Report the malaria status of this cell.
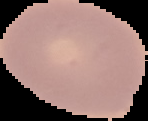
It is uninfected.

From a thin blood film. Image is 148×121 pixels. The area outside the segmented cell region is set to black.